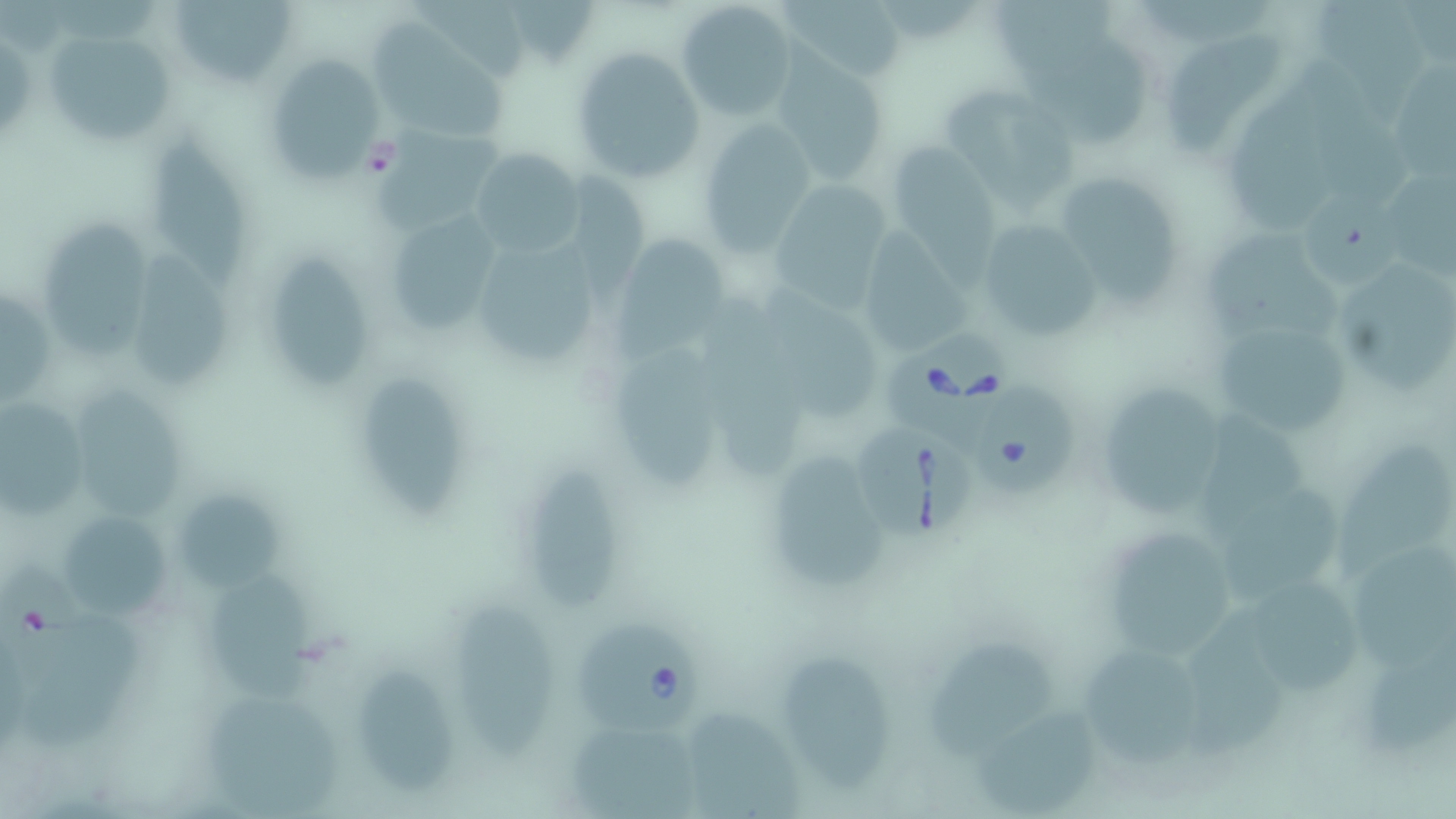

Approximate bounding boxes as [x1, y1, x2, y2] in pixels. Uninfected red blood cell locations: [170, 0, 294, 88], [783, 0, 911, 86], [1317, 0, 1428, 131], [997, 1, 1121, 69], [676, 2, 798, 119], [371, 19, 517, 143], [43, 27, 179, 148], [1168, 29, 1290, 153], [1017, 39, 1158, 144], [572, 47, 704, 185], [260, 51, 388, 187], [774, 59, 890, 187], [1231, 90, 1315, 229], [950, 97, 1080, 217], [699, 120, 817, 253], [369, 123, 500, 230], [151, 134, 242, 295], [887, 142, 999, 254], [471, 148, 581, 259], [1382, 164, 1456, 276], [565, 172, 657, 293], [1052, 172, 1183, 307], [771, 175, 892, 313], [1299, 188, 1390, 284], [393, 216, 506, 332], [973, 218, 1106, 343], [46, 219, 156, 364], [864, 225, 973, 351], [1205, 230, 1343, 339], [613, 233, 731, 356], [480, 244, 599, 358], [134, 246, 235, 386], [274, 254, 365, 388], [1337, 255, 1456, 397], [761, 286, 886, 417], [2, 287, 53, 407], [708, 301, 800, 476], [1209, 324, 1352, 435], [618, 347, 722, 491], [357, 376, 461, 519], [1084, 381, 1227, 527], [75, 385, 183, 520], [0, 400, 90, 519], [1202, 408, 1312, 533], [1329, 435, 1456, 566], [777, 449, 892, 584], [527, 464, 628, 612], [1221, 490, 1338, 606], [180, 497, 288, 596], [55, 503, 180, 628], [1109, 532, 1236, 659], [1349, 537, 1456, 663], [211, 579, 323, 704], [1259, 587, 1360, 696], [457, 602, 563, 763], [1186, 612, 1289, 753], [21, 617, 149, 753], [927, 635, 1058, 757], [1085, 643, 1195, 767], [778, 645, 885, 791], [1370, 646, 1456, 759], [362, 659, 455, 792], [204, 689, 338, 819], [970, 706, 1099, 813], [690, 712, 794, 819], [570, 722, 696, 819]. Babesia divergens-infected red blood cell locations: [882, 332, 1016, 443], [973, 385, 1077, 496], [858, 424, 975, 539], [0, 564, 89, 686], [580, 626, 705, 734]. Slide-level diagnosis: Babesia divergens. Thin blood smear. Optical microscopy. Image is 1456×819 pixels. Captured at 1000x magnification. Single field of view. May-Grünwald-Giemsa stain.